Name the parasite shown.
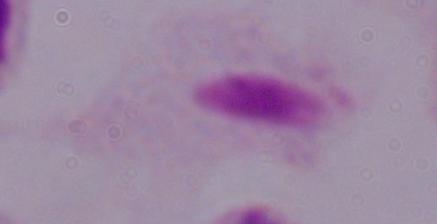

This is a trichomonad.

modality: micrograph
magnification: 1000x